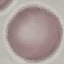

Summary:
  - Result: no malaria parasites detected
  - Image type: automatically extracted cell patch, resized to 64 × 64 pixels
  - Stain: Giemsa
  - Preparation: thin blood smear
  - Capture: smartphone camera at the microscope eyepiece